Identify the blood parasite species.
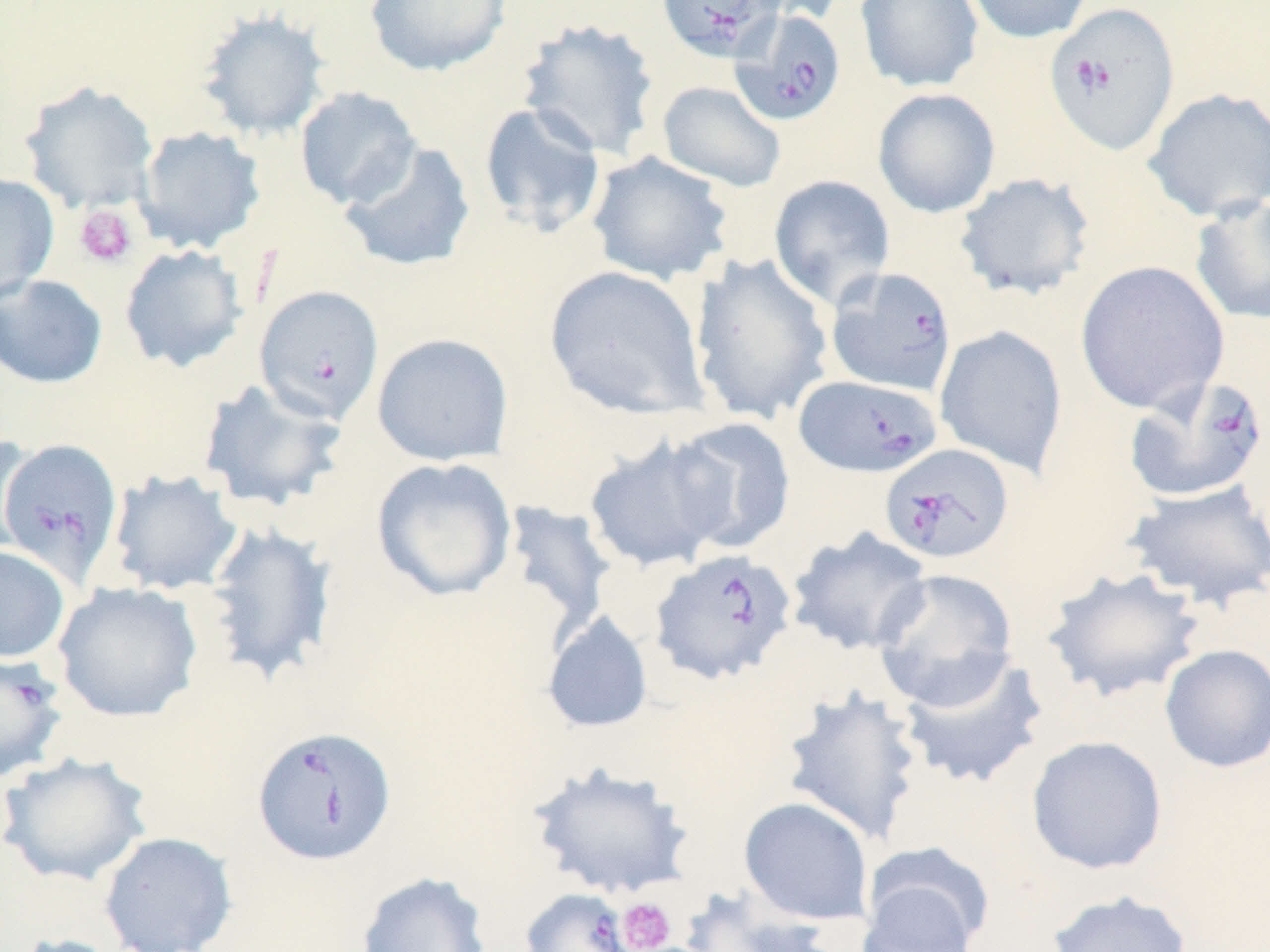

Babesia divergens.

Summary:
  - Coordinate format: approximate bounding boxes as (x1,y1)-(x2,y2) corner pairs in pixels
  - Babesia divergens-infected red blood cell locations: (657,0)-(790,60), (1043,2)-(1181,157), (729,9)-(847,126), (825,267)-(958,397), (255,285)-(385,424), (793,374)-(942,478), (1124,374)-(1269,503), (0,436)-(122,588), (878,443)-(1015,565), (648,549)-(797,686), (0,658)-(55,789), (251,724)-(397,866), (519,887)-(639,952)
  - Uninfected red blood cell locations: (364,0)-(513,77), (737,0)-(848,24), (854,0)-(984,93), (962,0)-(1094,44), (195,7)-(332,142), (516,17)-(661,162), (19,81)-(158,214), (656,81)-(786,192), (294,86)-(422,210), (1142,87)-(1270,222), (872,88)-(1001,219), (478,101)-(607,239), (134,125)-(266,255), (338,140)-(476,273), (586,150)-(734,286), (953,172)-(1096,301), (0,174)-(60,303), (768,174)-(896,308), (1190,194)-(1270,327), (119,244)-(249,373), (689,252)-(835,426), (1074,260)-(1230,415), (543,264)-(709,420), (0,274)-(108,389), (934,324)-(1068,478), (371,333)-(514,466), (196,378)-(349,515), (665,417)-(796,554), (583,434)-(732,574), (0,435)-(40,556), (371,457)-(517,602), (107,469)-(243,596), (1123,479)-(1270,611), (497,500)-(616,640), (202,521)-(339,686), (786,526)-(934,656), (0,545)-(70,663), (1040,566)-(1208,704), (872,568)-(1019,709), (52,581)-(203,722), (541,610)-(654,734), (1159,644)-(1270,773), (894,650)-(1050,790), (779,686)-(925,846), (1026,735)-(1168,875), (1,752)-(154,887), (528,761)-(696,900), (738,796)-(874,926), (98,831)-(238,952), (859,848)-(990,952), (355,871)-(493,952), (677,887)-(832,952), (1045,888)-(1193,952), (5,934)-(131,952)
  - Platelet locations: (74,204)-(137,268), (617,897)-(676,952)
  - Field of view: one of a larger specimen
  - Stain: May-Grünwald-Giemsa
  - Image size: 1270×952 pixels
  - Preparation: thin blood smear
  - Magnification: 1000x
  - Modality: optical microscopy